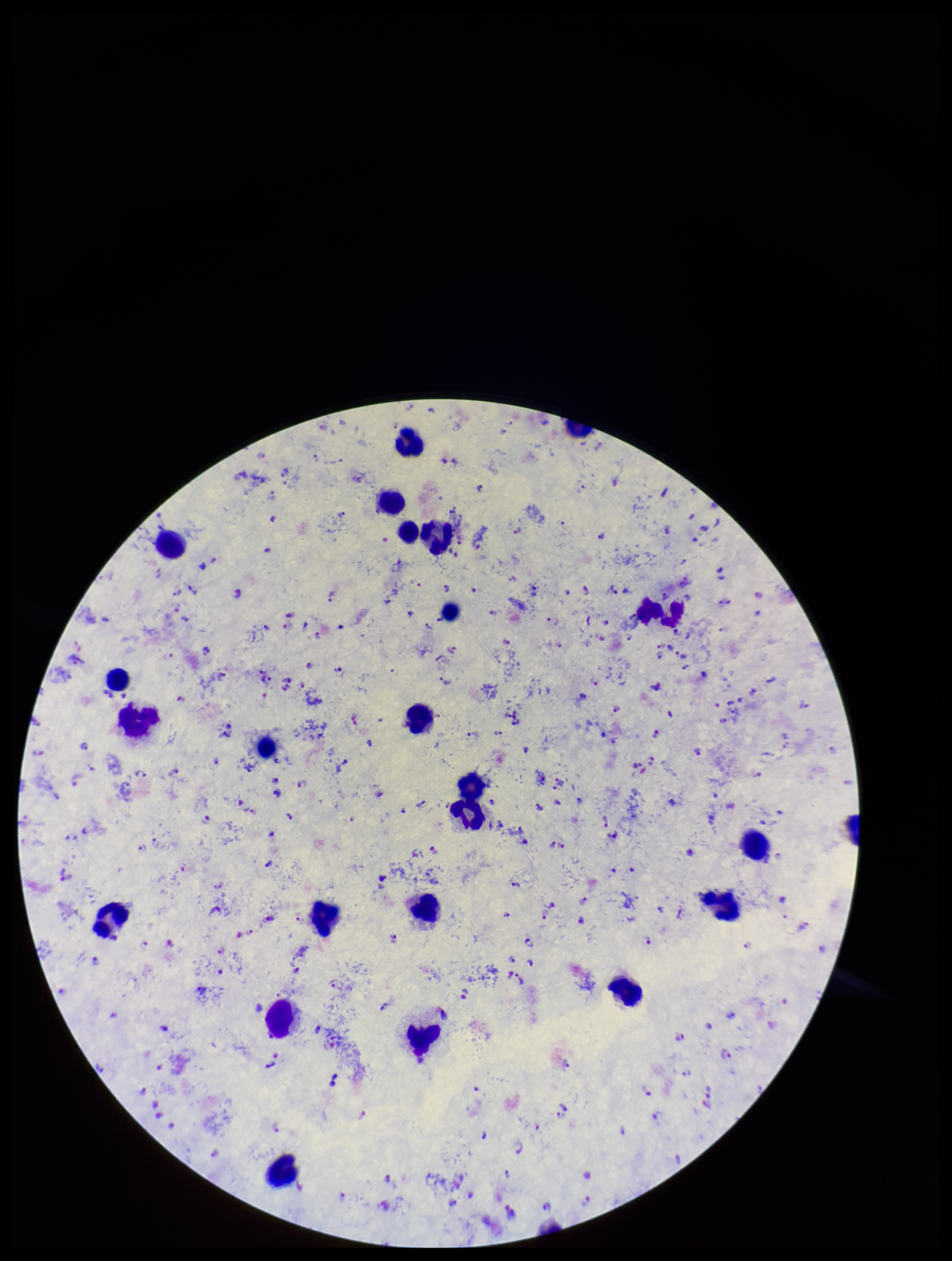 Species reported for this patient: Plasmodium falciparum. Image is 952×1261 pixels. Photographed through the microscope eyepiece with a smartphone camera. Stained with Giemsa. One field from this slide. Leukocyte count: 24. Preparation: thick. Parasite count: 250. Plasmodium parasites: detected. Patient malaria status: positive.